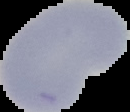

malaria status = uninfected
preparation = thin blood film
image size = 130×112 pixels
image type = segmented cell region with the area outside set to black